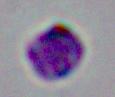
1000x magnification. A Leishmania parasite is shown. Photomicrograph.